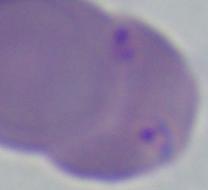

magnification = 1000x
modality = photomicrograph
identification = Babesia